Locate every malaria parasite.
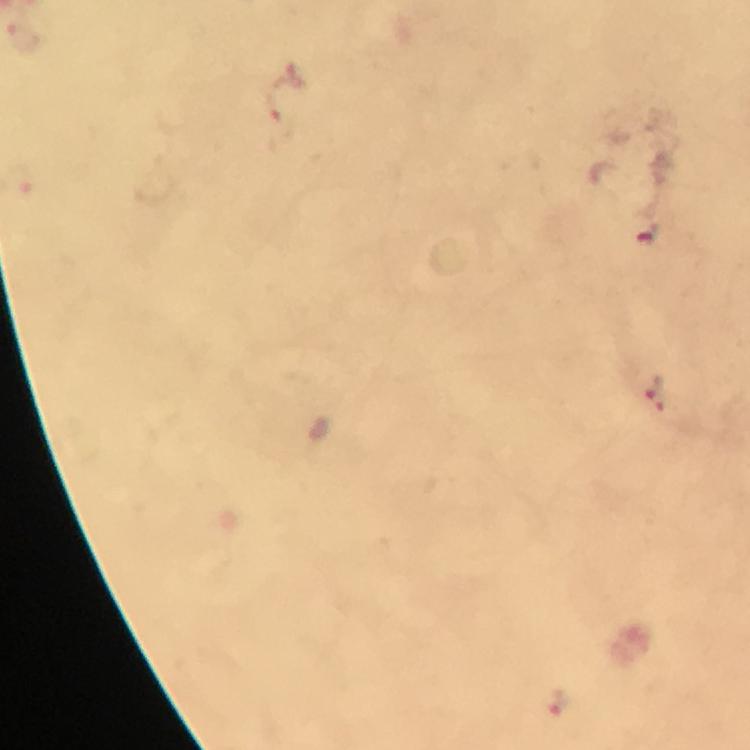
Approximate centers as [x, y] in pixels.
Malaria parasites: [647, 231], [657, 394], [557, 703].

{
  "capture": "smartphone camera through the microscope",
  "magnification": "100x",
  "immersion_oil": "applied",
  "cropped_from": "one field of view",
  "image_size": "750×750 pixels",
  "context": "from a diagnostic examination for malaria",
  "preparation": "thick blood smear",
  "stain": "Giemsa"
}